Identify the parasite.
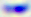
Toxoplasma gondii.

Summary:
  - Magnification: 400x
  - Modality: photomicrograph